Assess this cell for malaria.
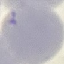
Uninfected.

Cell patch, automatically extracted from a larger field of view and resized to 64 × 64 pixels. Giemsa stain. Thin blood smear. Acquired by smartphone through the microscope eyepiece.